Locate every blood parasite and identify its species.
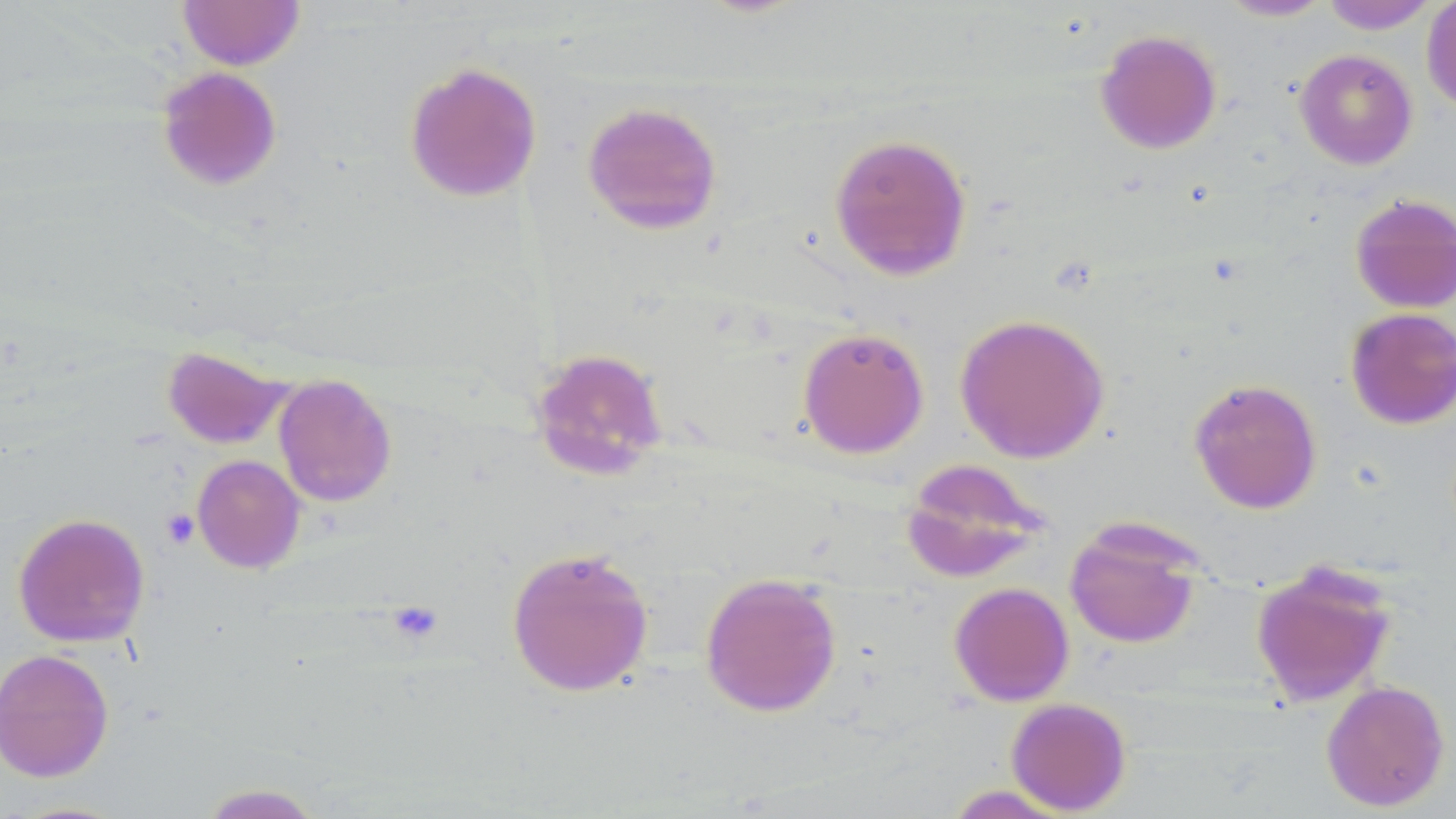

No blood parasites seen.

Summary:
  - Coordinate format: approximate bounding boxes as (x1, y1, x2, y2) in pixels
  - Platelet locations: (161, 508, 200, 549), (386, 600, 444, 644)
  - Uninfected red blood cell locations: (176, 0, 305, 70), (1216, 0, 1334, 22), (1318, 0, 1441, 33), (1421, 0, 1456, 114), (1094, 28, 1222, 155), (1294, 49, 1418, 170), (403, 60, 543, 203), (155, 66, 283, 192), (581, 101, 723, 235), (829, 133, 972, 281), (1350, 193, 1456, 313), (1345, 307, 1456, 429), (954, 313, 1110, 463), (797, 326, 929, 459), (161, 345, 292, 449), (527, 347, 669, 482), (273, 374, 397, 507), (1188, 377, 1323, 514), (191, 454, 306, 574), (901, 457, 1048, 582), (12, 512, 150, 648), (1064, 518, 1205, 649), (505, 546, 655, 697), (1250, 558, 1399, 707), (699, 571, 842, 717), (948, 582, 1074, 706), (0, 648, 114, 782), (1321, 679, 1450, 812), (1005, 697, 1132, 815), (196, 782, 328, 818), (942, 785, 1075, 818)
  - Slide-level diagnosis: no evidence of blood parasites
  - Magnification: 1000x
  - Image size: 1456×819 pixels
  - Stain: May-Grünwald-Giemsa
  - Modality: optical microscopy
  - Field of view: one of a larger specimen
  - Preparation: thin blood film